State the preparation type.
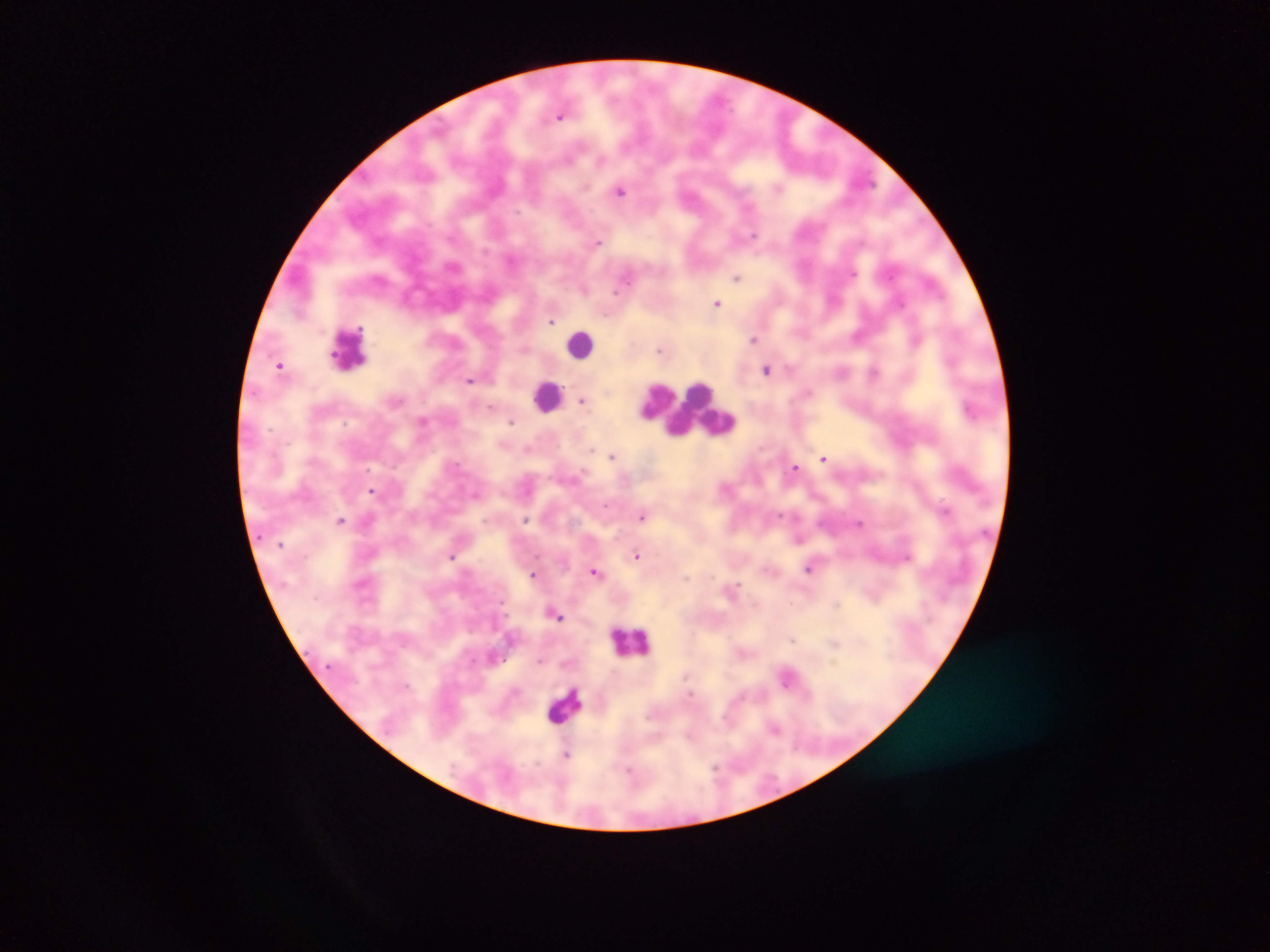
This is a thick smear.

Approximate centers as x y in pixels. Malaria parasite locations: 560 116; 600 160; 585 187; 620 191; 753 235; 597 241; 852 273; 737 277; 626 280; 616 291; 717 303; 551 321; 754 339; 916 341; 659 350; 280 365; 767 369; 873 372; 470 380; 583 401; 490 408; 422 420; 511 422; 591 449; 612 456; 824 458; 795 467; 372 491; 475 494; 606 505; 944 510; 779 515; 643 516; 526 519; 340 520; 859 523; 637 555; 451 556; 907 557; 809 569; 595 572; 533 573; 686 577; 558 616; 792 640; 834 643; 540 661; 787 679; 406 685; 690 695; 774 728; 566 755; 716 766. Leukocyte locations: 581 344; 348 348; 547 396; 689 410; 633 641; 566 704. Image is 1270×952 pixels. Collected in Ghana. Mobile-phone photograph taken through the microscope. Single field of view.